Classify this cell by malaria status.
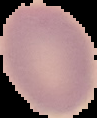

It is uninfected.

From a thin blood film. Image is 97×118 pixels. Segmented cell region on a black background.